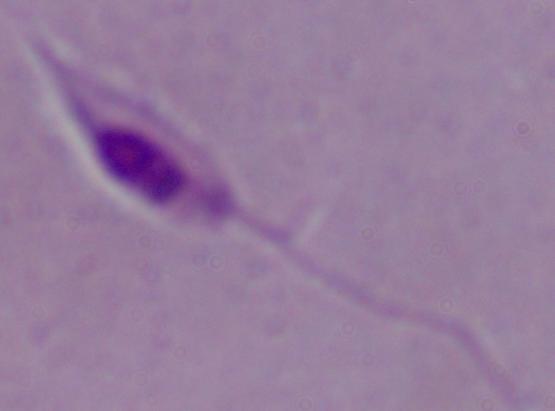

Summary:
  - Identification: Leishmania
  - Magnification: 1000x
  - Modality: micrograph